Identify the cell.
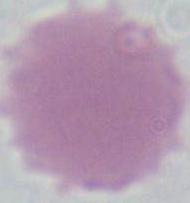
An erythrocyte.

Summary:
  - Modality: micrograph
  - Magnification: 1000x